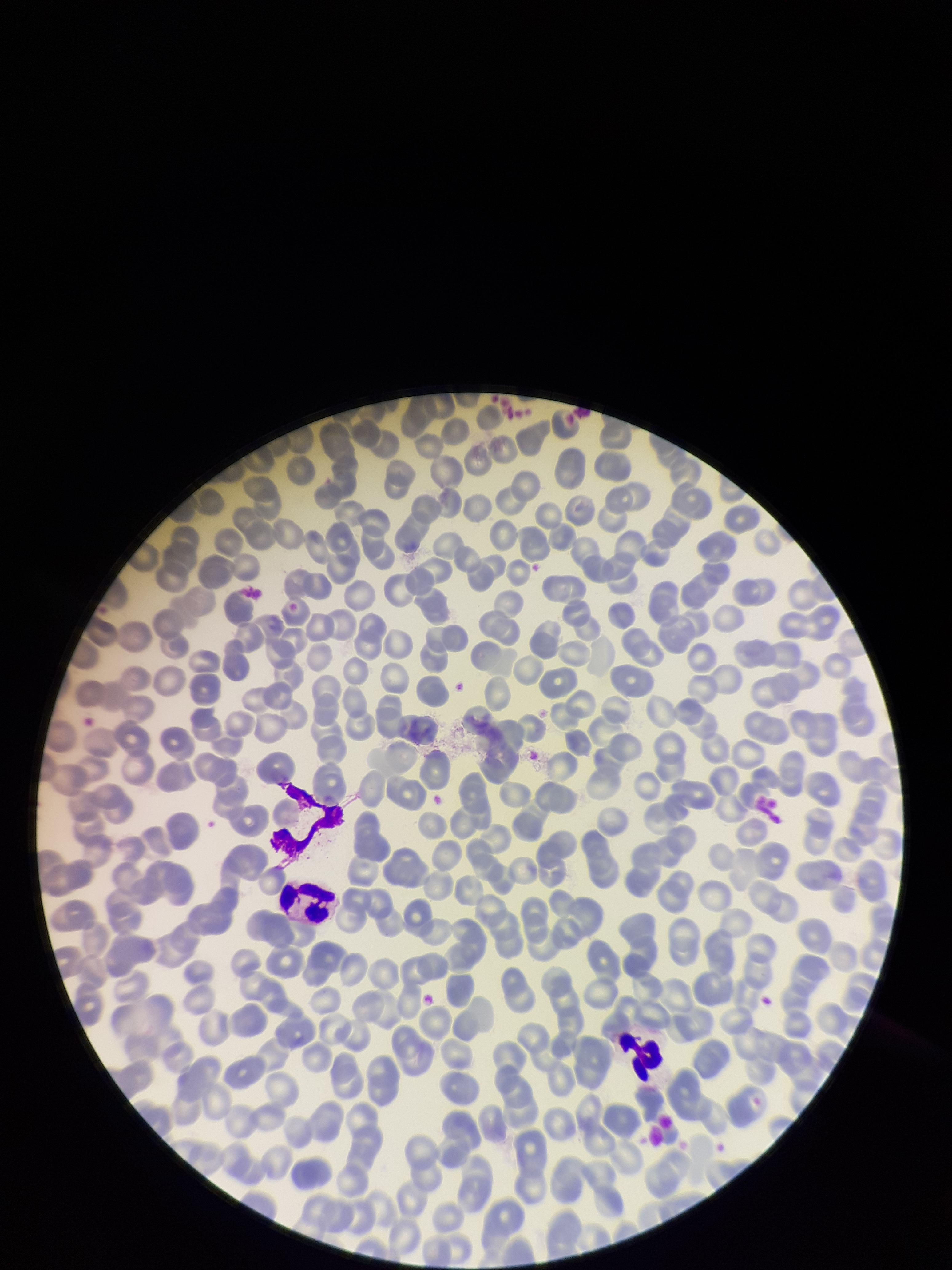
Summary:
  - Parasitized red blood cell count: 0
  - Patient malaria status: negative
  - Stain: Giemsa
  - Red blood cell count: 278
  - Parasitized red blood cells: none seen
  - Capture: smartphone photograph through the microscope eyepiece
  - Image size: 952×1270 pixels
  - Preparation: thin smear
  - Field of view: one from this slide